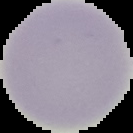
result = negative for Plasmodium parasites
image size = 133×133 pixels
image type = segmented cell region with the area outside set to black
preparation = thin blood smear